Locate every malaria parasite and every leukocyte.
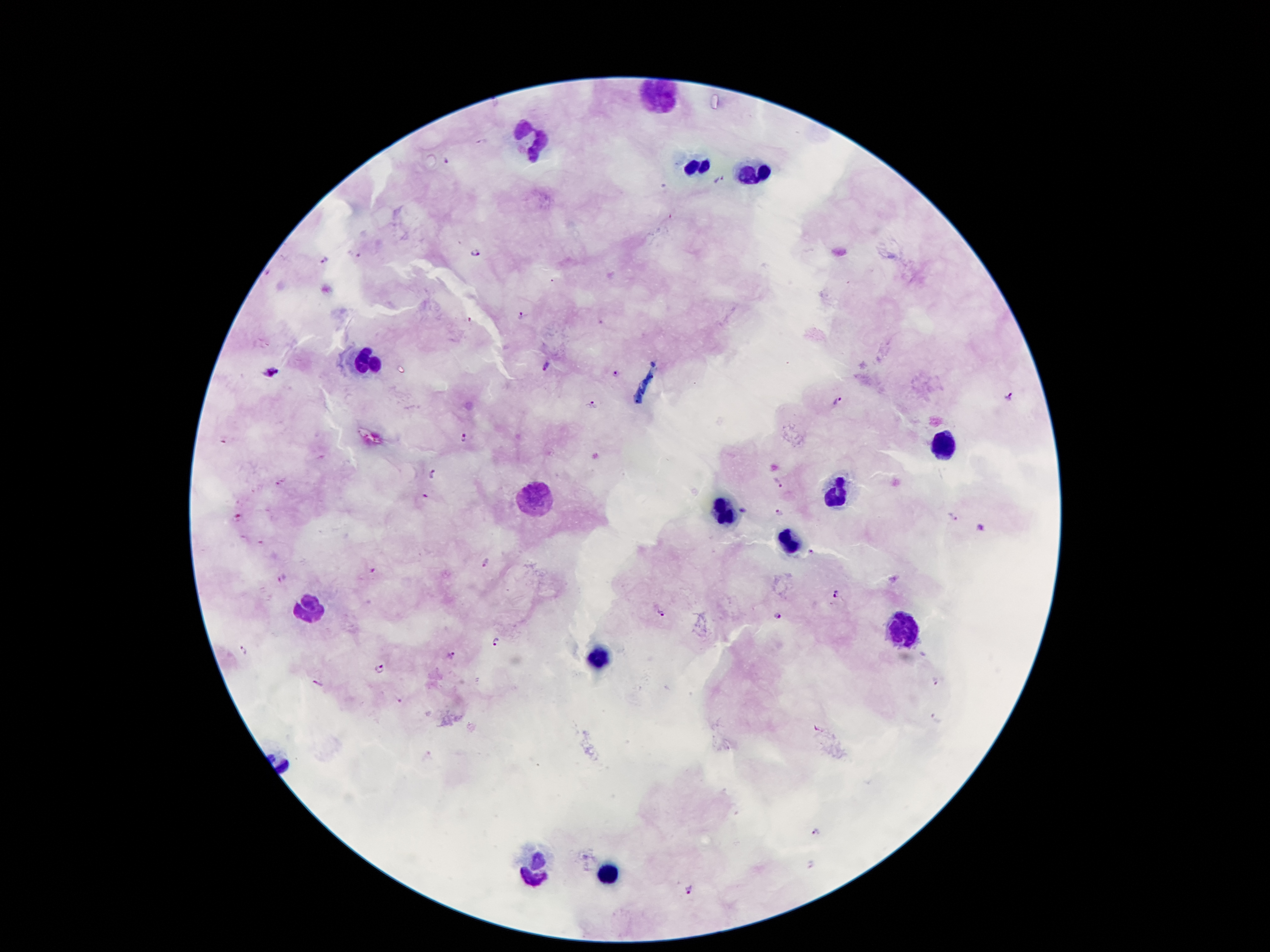
Approximate centers as {x, y} in pixels.
Malaria parasites: {448, 162}, {719, 180}, {475, 253}, {358, 254}, {324, 260}, {522, 317}, {546, 367}, {614, 372}, {270, 373}, {1008, 396}, {838, 402}, {591, 403}, {465, 437}, {434, 475}, {777, 482}, {426, 497}, {743, 508}, {779, 510}, {953, 518}, {981, 530}, {488, 563}, {284, 576}, {837, 595}, {660, 613}, {779, 615}, {499, 641}, {243, 652}, {452, 654}, {378, 668}, {937, 681}, {317, 683}, {399, 700}, {816, 833}, {691, 890}.
Leukocytes: {661, 98}, {532, 139}, {696, 165}, {752, 173}, {369, 360}, {944, 448}, {834, 494}, {534, 497}, {723, 514}, {790, 539}, {311, 607}, {905, 629}, {600, 656}, {535, 867}, {608, 875}.

image_size: 1270×952 pixels
capture: smartphone through the microscope eyepiece
field_of_view: single
preparation: thick blood film
magnification: 100x
patient_malaria_status: infected with Plasmodium falciparum
stain: Giemsa